Comment on the morphology of the red blood cells.
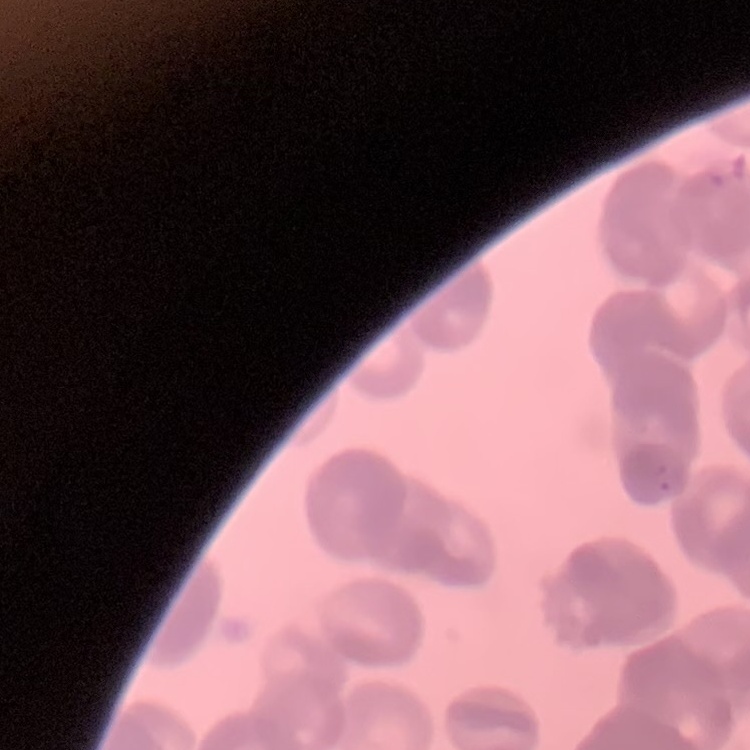
They show rouleaux formation.

Summary:
  - Stain: Field's or Giemsa
  - Preparation: thin peripheral smear
  - Image type: square crop of a larger photomicrograph